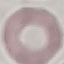

Summary:
  - Malaria status: uninfected
  - Stain: Giemsa
  - Capture: smartphone through the microscope eyepiece
  - Image type: cell patch, automatically extracted from a larger field of view and resized to 64 × 64 pixels
  - Preparation: thin blood smear